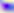

modality = micrograph
identification = Toxoplasma gondii
magnification = 400x